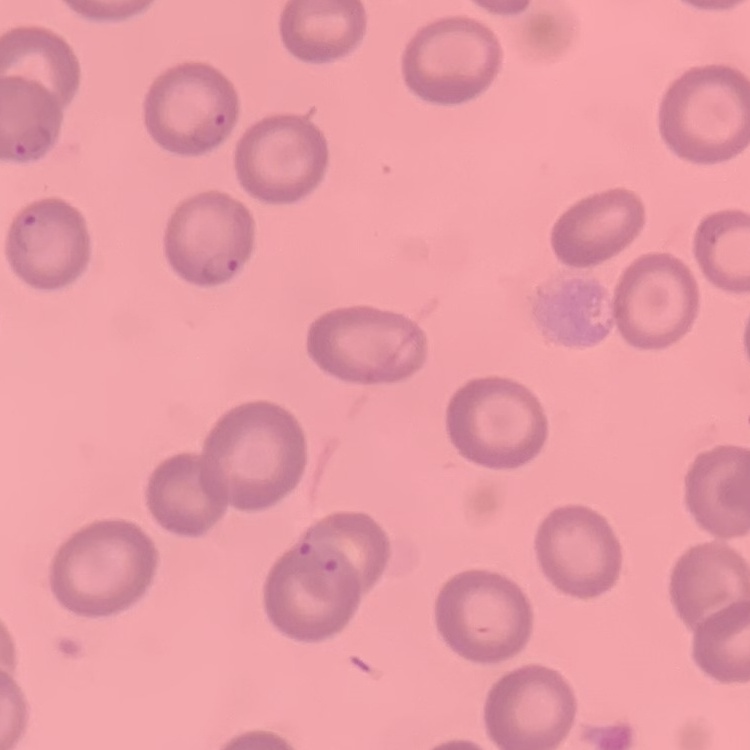

{
  "red_blood_cell_morphology": "no rouleaux formation",
  "image_type": "square crop of a larger photomicrograph",
  "preparation": "thin blood film",
  "stain": "Field's or Giemsa"
}